Identify the parasite.
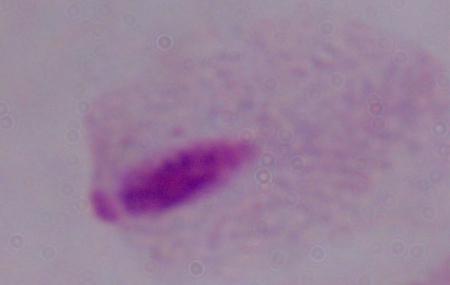
A trichomonad.

Photomicrograph. Captured at 1000x magnification.